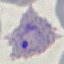
malaria status = parasitized
capture = smartphone through the microscope eyepiece
image type = cell patch, automatically extracted from a larger field of view and resized to 64 × 64 pixels
stain = Giemsa
preparation = thin blood smear